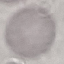
{
  "malaria_status": "uninfected",
  "preparation": "thin smear",
  "image_type": "cell patch, automatically extracted from a larger field of view and resized to 64 × 64 pixels",
  "stain": "Giemsa",
  "capture": "smartphone camera at the microscope eyepiece"
}